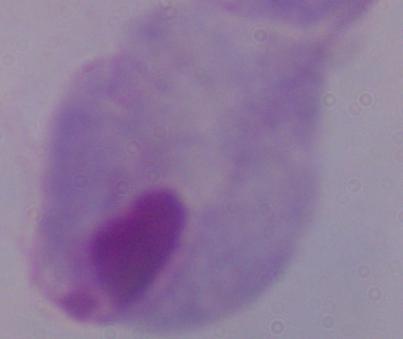

Captured at 1000x magnification. A trichomonad is seen. Micrograph.